Assess the morphology of the red blood cells.
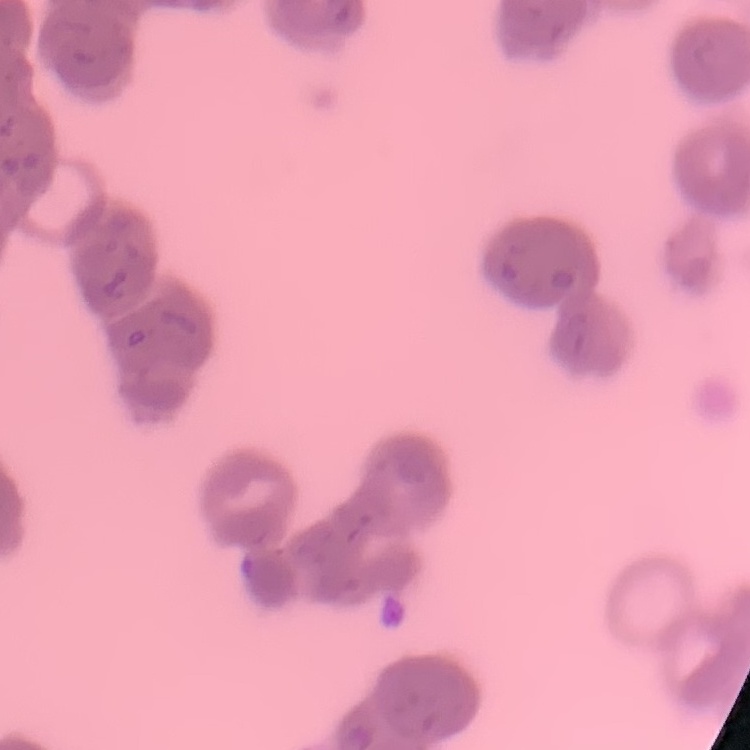
They show rouleaux formation.

One tile cut from a larger photomicrograph. Field's or Giemsa stain. Thin peripheral smear.